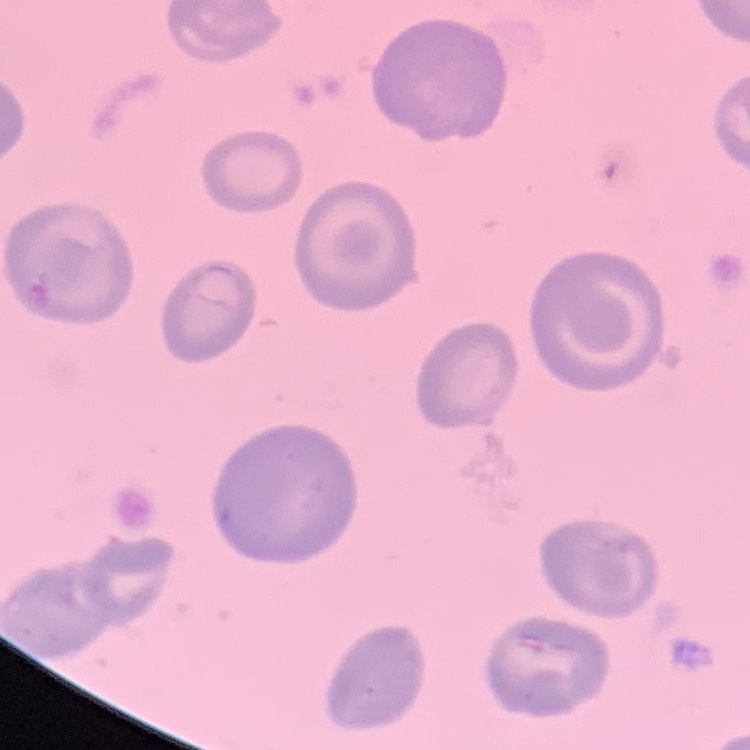

erythrocyte morphology = no rouleaux formation
image type = one tile cut from a larger photomicrograph
stain = Field's or Giemsa
preparation = thin blood smear